Outline each uninfected red blood cell.
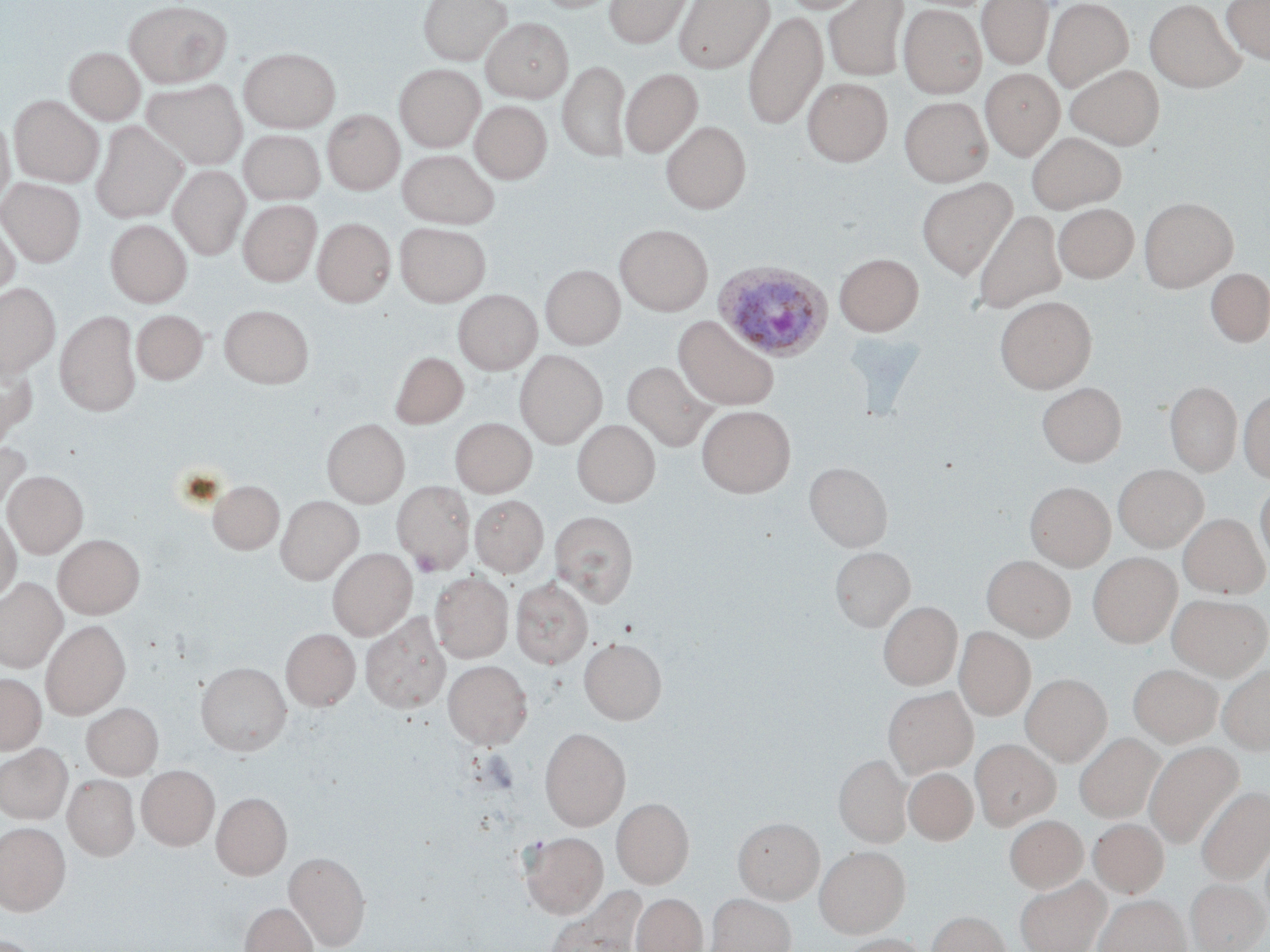

Approximate bounding boxes as (x1, y1, x2, y2) in pixels.
Uninfected red blood cells: (418, 0, 511, 64), (604, 0, 693, 47), (674, 0, 773, 72), (781, 0, 871, 14), (823, 0, 909, 81), (978, 0, 1054, 69), (1044, 0, 1133, 90), (1145, 0, 1246, 92), (1222, 0, 1270, 63), (125, 1, 231, 87), (898, 4, 987, 97), (744, 10, 827, 130), (482, 18, 572, 102), (64, 47, 145, 125), (239, 48, 340, 133), (558, 59, 631, 162), (395, 64, 485, 150), (1066, 64, 1164, 149), (980, 67, 1064, 159), (621, 68, 703, 157), (803, 77, 892, 166), (142, 79, 247, 169), (10, 96, 103, 187), (899, 96, 992, 186), (471, 100, 552, 183), (322, 110, 404, 195), (0, 113, 14, 208), (91, 121, 187, 223), (661, 121, 751, 214), (239, 128, 325, 205), (1026, 131, 1126, 213), (398, 149, 499, 228), (169, 165, 251, 260), (0, 178, 85, 266), (917, 178, 1017, 278), (1139, 197, 1237, 291), (238, 199, 321, 286), (1053, 203, 1139, 282), (973, 209, 1066, 314), (0, 216, 20, 301), (312, 218, 396, 307), (105, 220, 192, 306), (395, 223, 491, 306), (616, 225, 712, 315), (835, 253, 923, 335), (540, 264, 625, 349), (1204, 268, 1270, 348), (0, 283, 60, 376), (454, 289, 541, 375), (996, 296, 1096, 393), (219, 305, 313, 388), (132, 309, 208, 385), (55, 311, 141, 415), (675, 315, 778, 410), (514, 350, 607, 448), (391, 352, 468, 428), (0, 356, 36, 444), (622, 360, 716, 452), (1165, 381, 1241, 475), (1037, 382, 1126, 466), (1239, 388, 1270, 483), (696, 405, 796, 497), (450, 418, 537, 497), (322, 419, 409, 507), (573, 419, 660, 506), (0, 441, 31, 517), (805, 462, 892, 550), (1113, 465, 1208, 551), (3, 470, 88, 558), (1255, 479, 1270, 570), (209, 480, 284, 553), (392, 481, 475, 574), (1025, 481, 1115, 571), (469, 495, 548, 577), (275, 496, 363, 583), (550, 510, 638, 607), (0, 511, 21, 604), (1180, 513, 1269, 598), (53, 534, 145, 618), (831, 546, 915, 630), (327, 548, 416, 640), (1088, 552, 1181, 647), (982, 555, 1075, 640), (430, 572, 513, 662), (0, 578, 66, 672), (510, 578, 593, 668), (1167, 593, 1269, 679), (879, 600, 962, 689), (362, 613, 449, 713), (41, 620, 130, 718), (955, 627, 1035, 720), (281, 628, 360, 711), (579, 638, 666, 723), (443, 660, 532, 749), (196, 661, 291, 754), (1128, 663, 1222, 747), (1218, 664, 1270, 755), (0, 672, 46, 754), (1021, 673, 1111, 765), (884, 687, 976, 777), (82, 703, 163, 779), (540, 727, 630, 829), (1075, 732, 1164, 823), (971, 739, 1059, 828), (1145, 742, 1244, 848), (0, 744, 72, 824), (834, 754, 911, 845), (137, 765, 219, 851), (903, 767, 978, 845), (63, 774, 140, 860), (1197, 786, 1270, 885), (212, 792, 291, 879), (612, 798, 694, 888), (1005, 815, 1087, 892), (734, 817, 824, 903), (1089, 818, 1168, 897), (0, 822, 71, 914), (520, 831, 608, 917), (815, 846, 909, 937), (284, 851, 369, 949), (1015, 877, 1110, 952), (1186, 878, 1268, 952), (544, 887, 647, 952), (632, 893, 707, 952), (706, 893, 795, 952), (1094, 894, 1189, 952), (240, 902, 317, 952), (927, 911, 1011, 952), (0, 934, 45, 952), (836, 934, 932, 952).

Plasmodium ovale-infected red blood cell locations: (713, 259, 832, 361). Platelet locations: (412, 551, 442, 577). Slide-level diagnosis: Plasmodium ovale. Image is 1270×952 pixels. May-Grünwald-Giemsa stain. Thin blood film. Single field of view. Captured at 1000x magnification. Light microscopy.